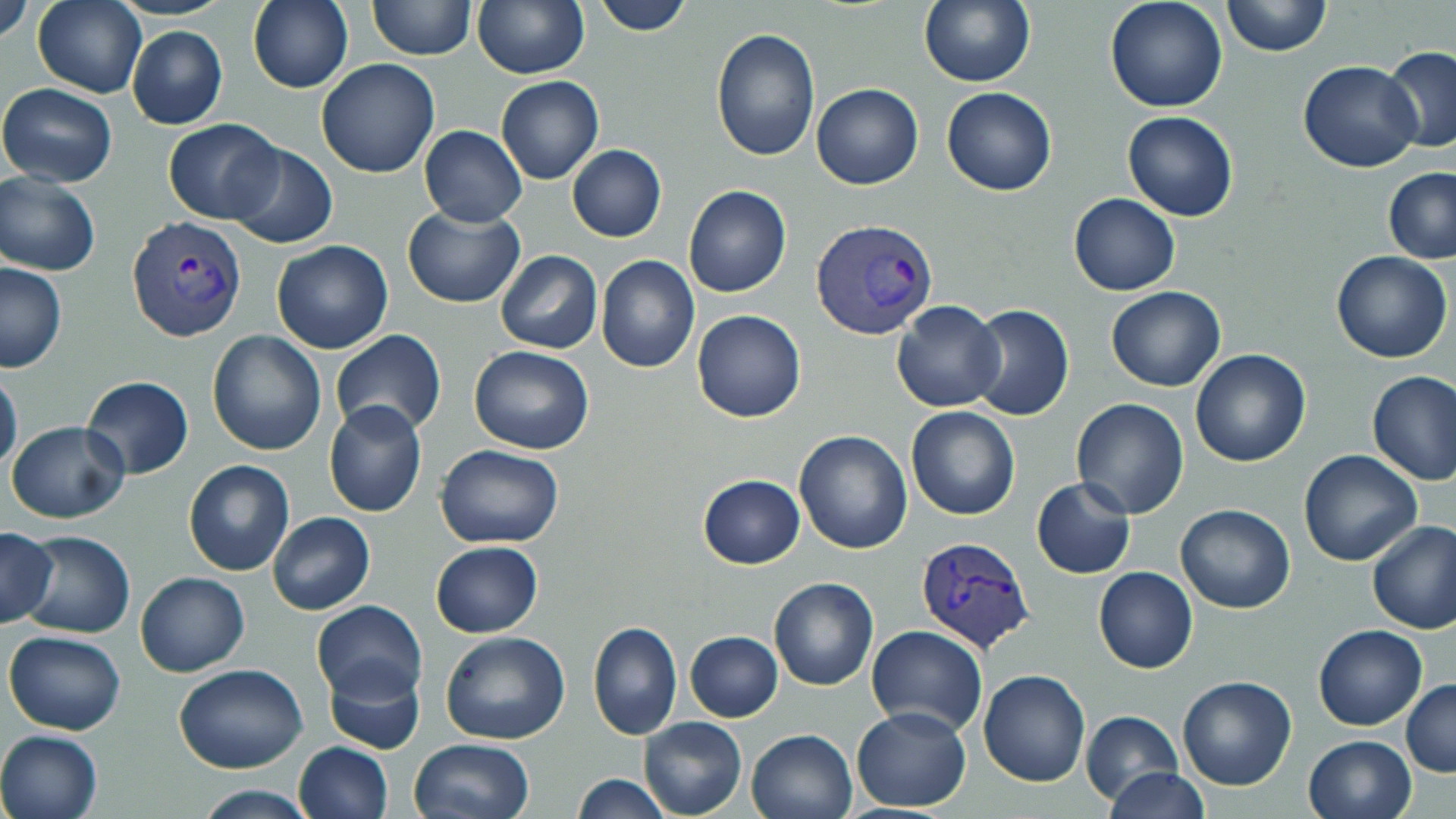
Approximate bounding boxes as [x1, y1, x2, y2] in pixels. Uninfected red blood cell locations: [1, 0, 33, 48], [34, 0, 145, 98], [247, 0, 354, 94], [367, 0, 476, 59], [473, 0, 588, 78], [592, 0, 694, 35], [919, 0, 1034, 87], [1104, 0, 1229, 113], [1222, 0, 1331, 57], [39, 12, 227, 117], [126, 27, 227, 129], [709, 27, 821, 162], [1379, 45, 1456, 156], [315, 58, 439, 178], [1297, 60, 1422, 171], [496, 77, 603, 185], [0, 83, 117, 187], [812, 83, 924, 189], [941, 86, 1057, 196], [1121, 111, 1239, 221], [163, 119, 285, 222], [419, 125, 526, 227], [226, 142, 338, 248], [567, 145, 666, 243], [1382, 168, 1456, 265], [1, 175, 101, 275], [683, 187, 792, 298], [1068, 193, 1181, 296], [403, 207, 526, 308], [271, 239, 393, 354], [494, 250, 601, 354], [1331, 250, 1453, 363], [596, 256, 701, 373], [0, 262, 68, 374], [1105, 285, 1226, 394], [892, 300, 1004, 413], [969, 305, 1075, 421], [692, 310, 806, 423], [330, 330, 447, 441], [206, 331, 327, 457], [469, 345, 596, 455], [1188, 349, 1311, 467], [0, 370, 23, 476], [1366, 370, 1456, 486], [79, 376, 194, 479], [1070, 398, 1190, 519], [323, 401, 427, 518], [906, 405, 1020, 521], [5, 420, 129, 523], [794, 429, 912, 554], [435, 444, 564, 547], [1298, 449, 1422, 566], [184, 460, 294, 575], [697, 474, 805, 568], [1031, 478, 1136, 579], [1174, 503, 1296, 613], [267, 511, 375, 614], [1367, 522, 1456, 634], [0, 526, 57, 628], [16, 530, 136, 638], [430, 541, 544, 637], [1094, 567, 1198, 674], [135, 572, 250, 676], [768, 576, 879, 690], [311, 599, 427, 703], [587, 621, 682, 741], [1312, 624, 1428, 731], [867, 625, 988, 738], [3, 630, 126, 735], [440, 631, 569, 744], [685, 632, 782, 721], [323, 656, 425, 754], [174, 663, 308, 773], [978, 671, 1090, 787], [1175, 676, 1298, 791], [1402, 678, 1456, 777], [851, 706, 971, 812], [1080, 710, 1182, 804], [639, 717, 747, 818], [747, 728, 858, 819], [0, 729, 103, 818], [1303, 734, 1416, 819], [409, 738, 535, 819], [294, 741, 394, 819], [1105, 767, 1211, 819], [571, 775, 672, 818], [192, 784, 320, 817]. Plasmodium vivax-infected red blood cell locations: [127, 214, 247, 342], [810, 217, 939, 342], [915, 537, 1036, 654]. Slide-level diagnosis: Plasmodium vivax. Image is 1456×819 pixels. May-Grünwald-Giemsa stain. 1000x magnification. Single field of view. Light microscopy. Thin blood smear.